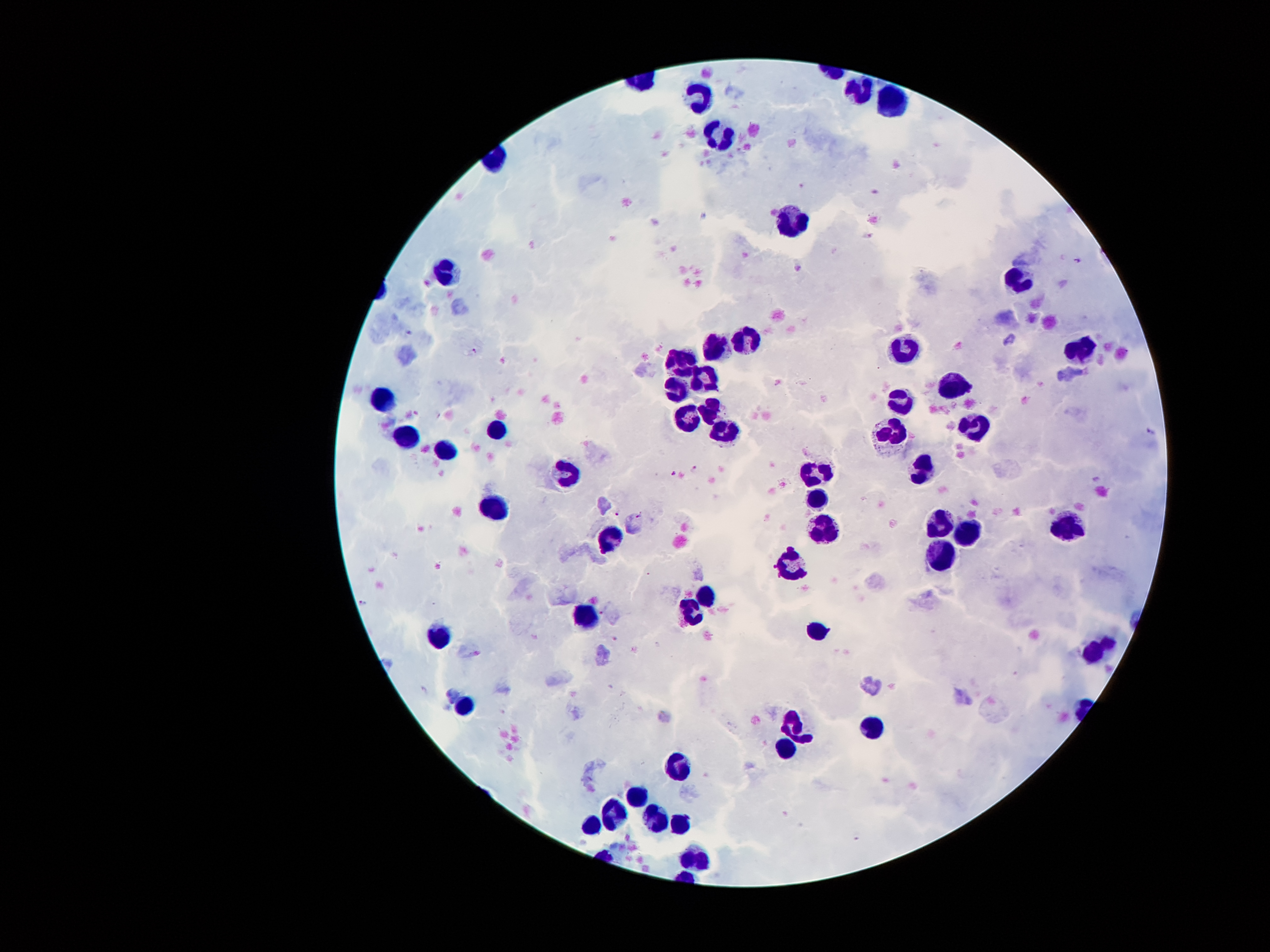
Approximate centers as (x, y) in pixels.
Summary:
  - Malaria parasite locations: (870, 235), (1080, 262), (472, 350), (1151, 432), (694, 470), (673, 474), (1095, 478), (617, 513), (639, 515), (363, 602), (600, 612)
  - Leukocyte locations: (856, 89), (892, 97), (694, 98), (722, 130), (793, 224), (449, 271), (1015, 280), (745, 339), (719, 344), (1081, 344), (908, 345), (675, 357), (707, 374), (954, 384), (671, 385), (901, 394), (383, 399), (711, 409), (686, 417), (722, 424), (976, 425), (494, 430), (403, 432), (890, 436), (443, 453), (924, 465), (814, 473), (564, 474), (819, 497), (491, 506), (941, 520), (826, 527), (1068, 530), (961, 531), (608, 537), (943, 552), (794, 559), (706, 592), (689, 611), (579, 617), (817, 631), (440, 640), (1094, 649), (465, 705), (792, 721), (875, 730), (783, 749), (682, 766), (635, 793), (616, 809), (657, 817), (679, 824), (587, 825), (697, 856)
  - Patient malaria status: infected with Plasmodium falciparum
  - Preparation: thick peripheral-blood smear
  - Image size: 1270×952 pixels
  - Field of view: one from this slide
  - Stain: Giemsa
  - Magnification: 100x
  - Capture: smartphone through the microscope eyepiece